Assess this cell for malaria.
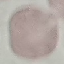
It is uninfected.

Acquired by smartphone through the microscope eyepiece. Giemsa stain. Thin blood film. Cell patch, automatically extracted from a larger field of view and resized to 64 × 64 pixels.